Report the malaria status.
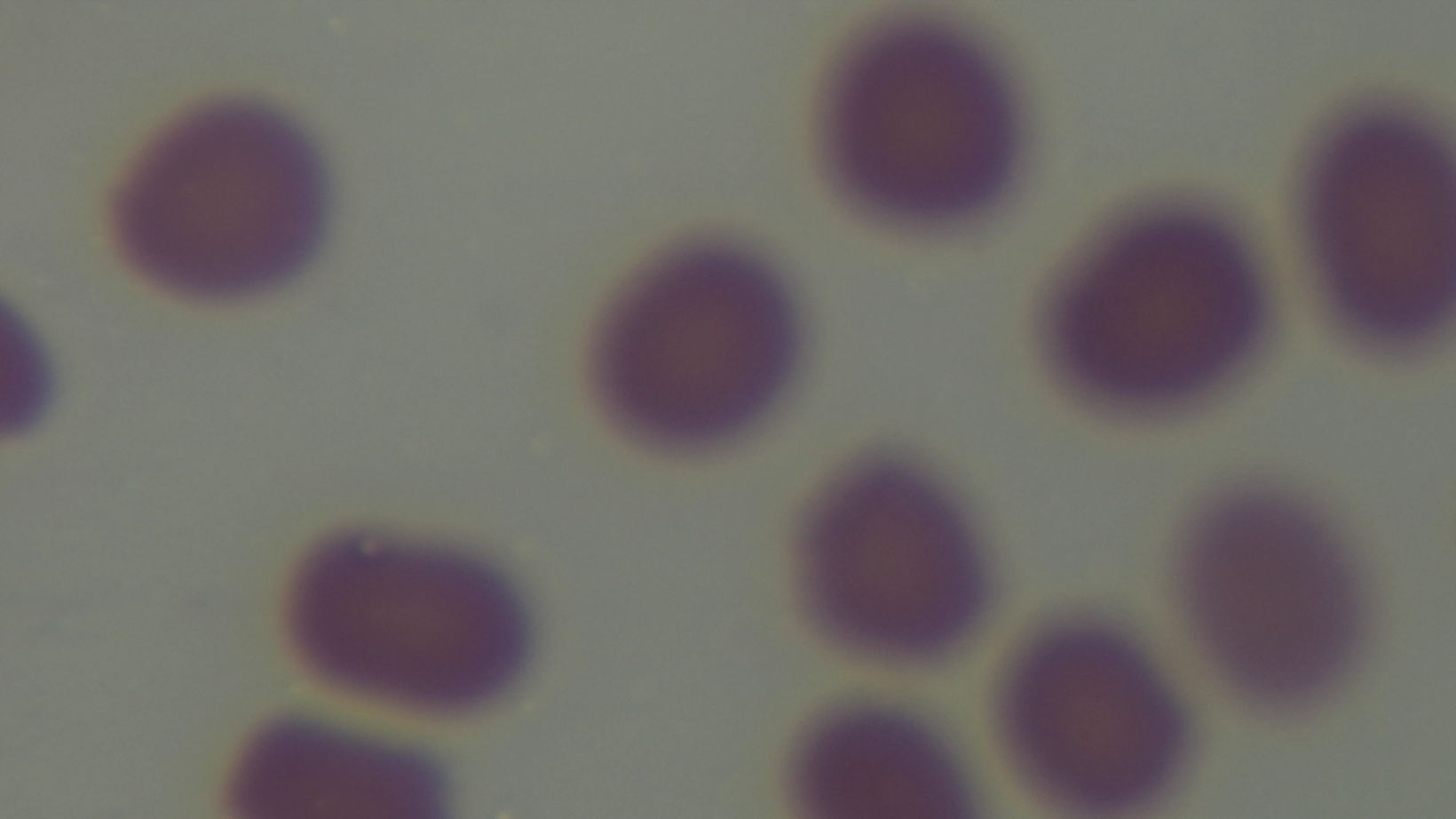

It is uninfected.

Giemsa stain. Preparation: thin blood film. Photomicrograph. Mounted 4K digital camera. Oil-immersion objective, 100x. One field from the slide.